Classify this cell by malaria status.
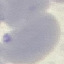

It is uninfected.

Summary:
  - Preparation: thin blood film
  - Stain: Giemsa
  - Image type: cell patch, automatically extracted from a larger field of view and resized to 64 × 64 pixels
  - Capture: smartphone camera at the microscope eyepiece